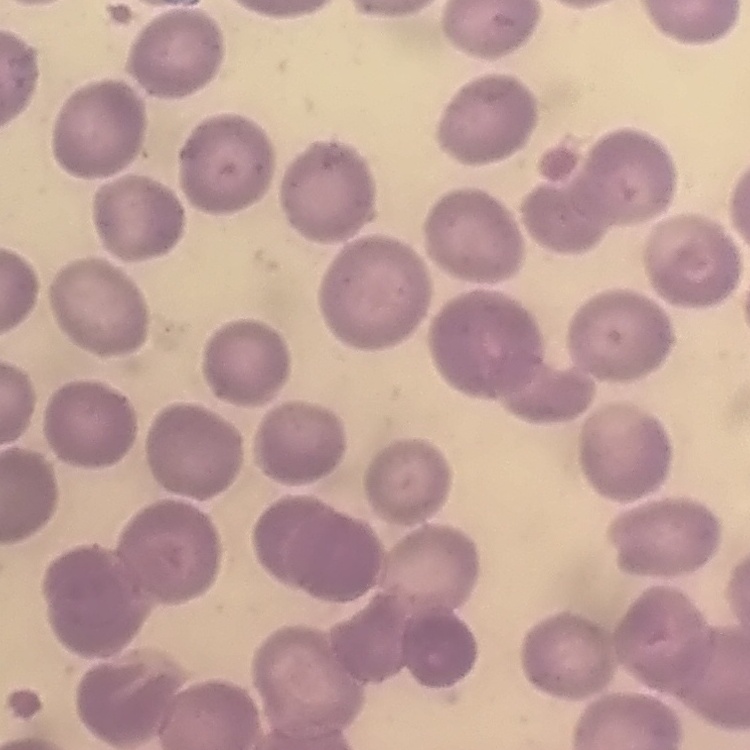

Summary:
  - Red blood cell morphology: no rouleaux formation
  - Preparation: thin blood film
  - Image type: one tile cut from a larger photomicrograph
  - Stain: Field's or Giemsa